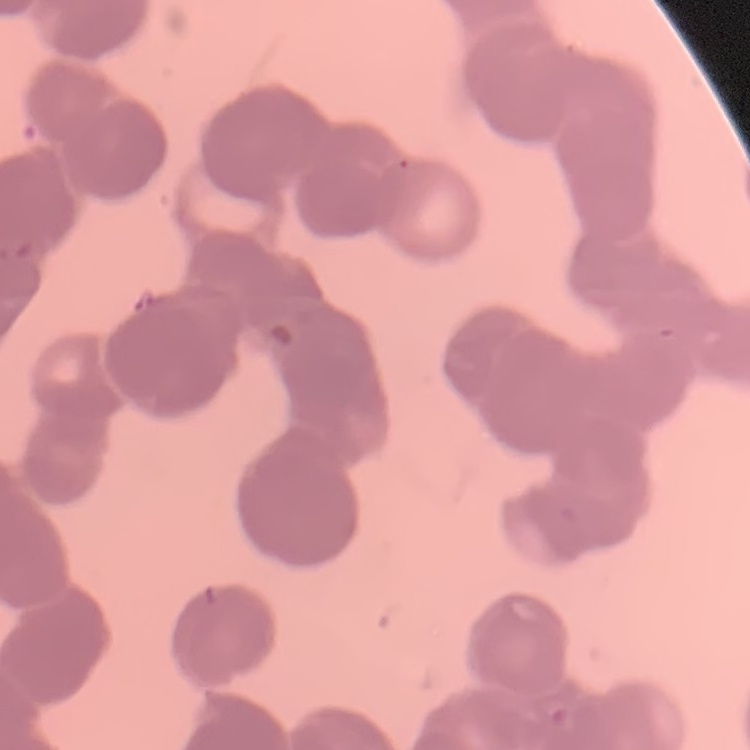

Summary:
  - Red blood cell morphology: rouleaux formation
  - Image type: one tile cut from a larger photomicrograph
  - Preparation: thin peripheral smear
  - Stain: Field's or Giemsa